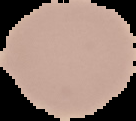
Summary:
  - Preparation: thin blood smear
  - Result: no malaria parasites detected
  - Image type: cell region segmented out of the field of view; surrounding area masked to black
  - Image size: 136×121 pixels